Locate and identify every blood parasite.
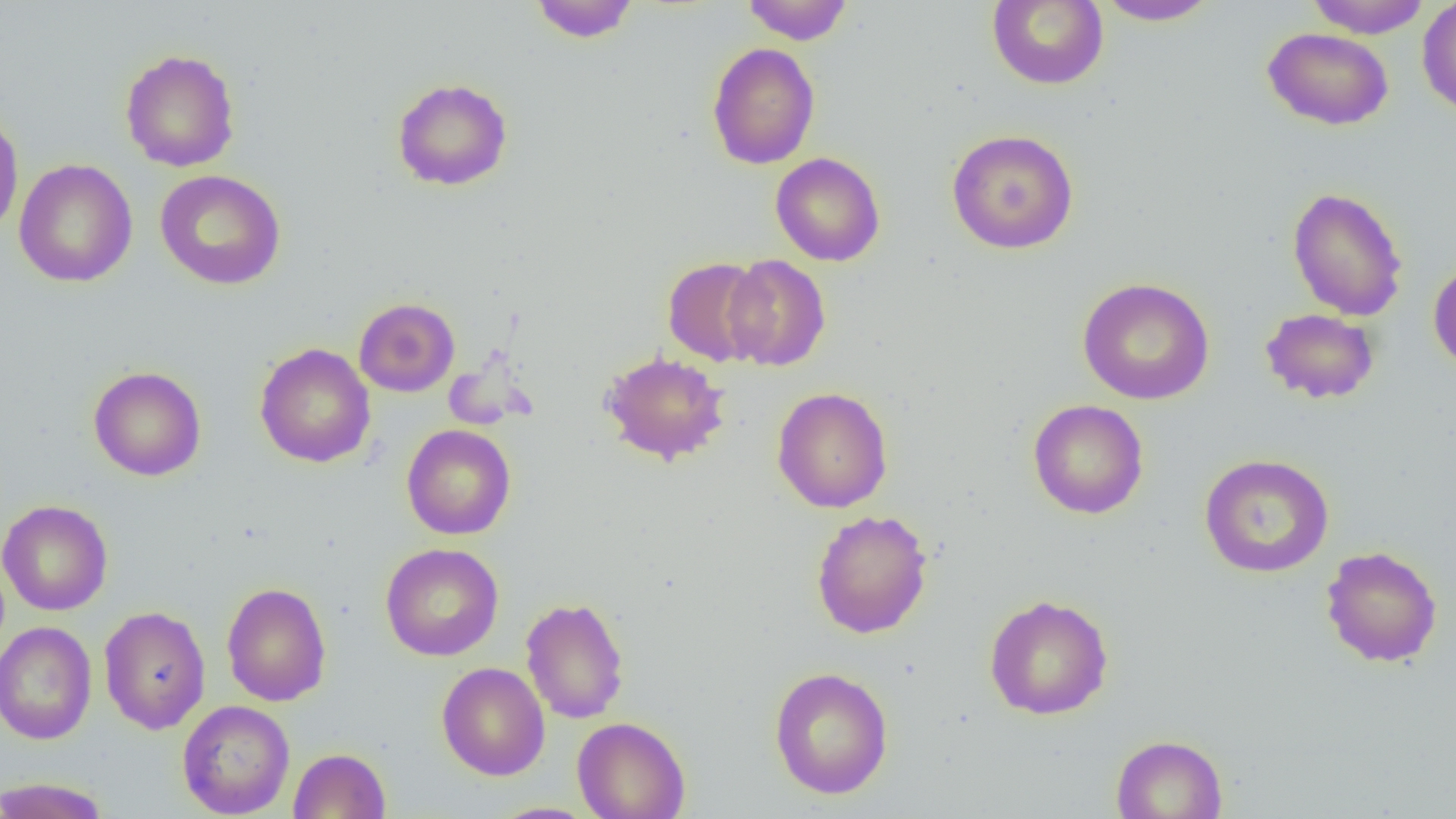
No blood parasites observed.

Approximate bounding boxes as (x1,y1)-(x2,y2) corner pairs in pixels. Uninfected red blood cell locations: (741,0)-(854,45), (987,0)-(1108,90), (1094,0)-(1222,26), (1305,0)-(1432,38), (1417,0)-(1456,118), (530,1)-(640,43), (1263,27)-(1393,130), (706,42)-(820,169), (120,48)-(240,172), (391,77)-(513,191), (0,109)-(24,240), (947,129)-(1079,254), (770,152)-(885,266), (13,159)-(138,287), (154,169)-(286,290), (1286,186)-(1409,321), (723,254)-(831,371), (662,257)-(768,366), (1428,259)-(1456,374), (1076,277)-(1215,404), (354,297)-(460,397), (1260,308)-(1380,404), (255,342)-(375,468), (599,350)-(731,466), (88,365)-(207,481), (771,387)-(893,512), (1028,399)-(1149,519), (401,424)-(516,540), (1199,453)-(1334,578), (0,499)-(113,616), (811,509)-(932,639), (379,542)-(504,661), (1320,545)-(1442,668), (222,581)-(332,706), (984,594)-(1114,720), (521,596)-(629,724), (98,605)-(211,734), (0,621)-(97,745), (436,662)-(550,780), (769,666)-(894,800), (177,700)-(295,818), (572,716)-(690,819), (1111,734)-(1228,819), (289,747)-(391,818), (0,776)-(111,818), (486,802)-(598,818). Slide-level diagnosis: negative for blood parasites. Light microscopy. Single field of view. Image is 1456×819 pixels. Thin blood film. Captured at 1000x magnification.